Point out each Plasmodium parasite.
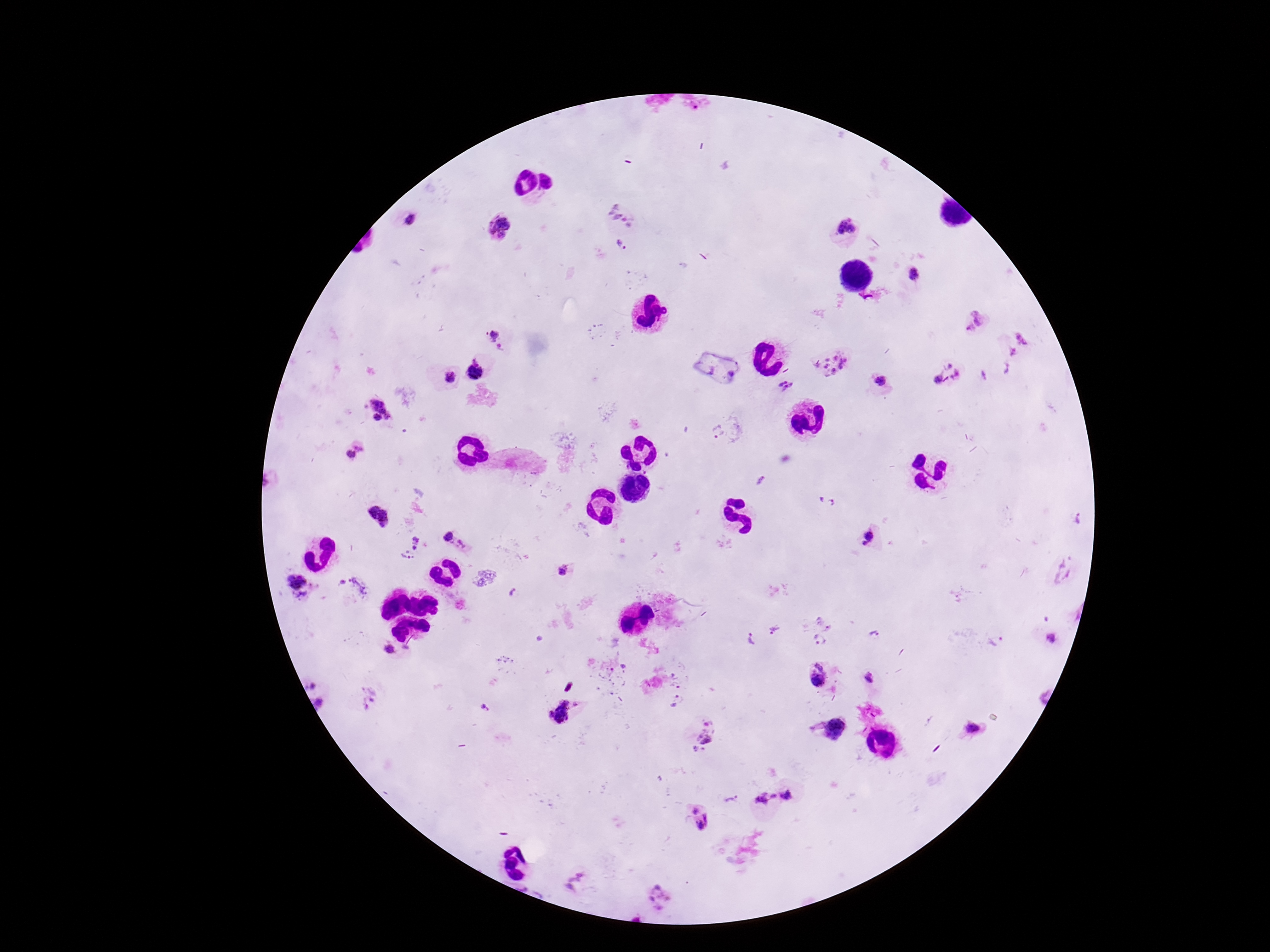
Approximate centers as (x, y) in pixels.
Plasmodium parasites: (623, 211), (406, 220), (499, 227), (848, 230), (624, 244), (914, 272), (973, 322), (498, 337), (834, 363), (477, 371), (947, 373), (449, 377), (881, 379), (787, 385), (378, 412), (717, 429), (354, 452), (759, 482), (378, 517), (447, 537), (869, 540), (417, 541), (462, 547), (405, 558), (564, 570), (1062, 572), (355, 587), (297, 589), (514, 594), (776, 629), (877, 636), (1055, 637), (996, 638), (751, 639), (821, 639), (390, 650), (504, 664), (816, 673), (675, 676), (869, 678), (369, 698), (677, 700), (319, 704), (483, 707), (561, 712), (831, 729), (971, 731), (704, 733), (792, 797), (764, 798), (732, 801), (699, 819), (576, 881), (655, 898).

stain: Giemsa
patient_malaria_status: infected
image_size: 1270×952 pixels
field_of_view: single
capture: smartphone camera through the microscope eyepiece
preparation: thick blood smear
magnification: 100x